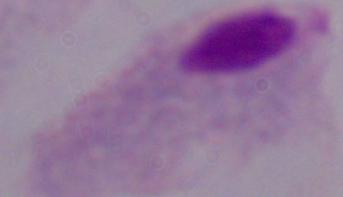

{
  "magnification": "1000x",
  "identification": "trichomonad",
  "modality": "photomicrograph"
}